Describe the morphology of the red blood cells.
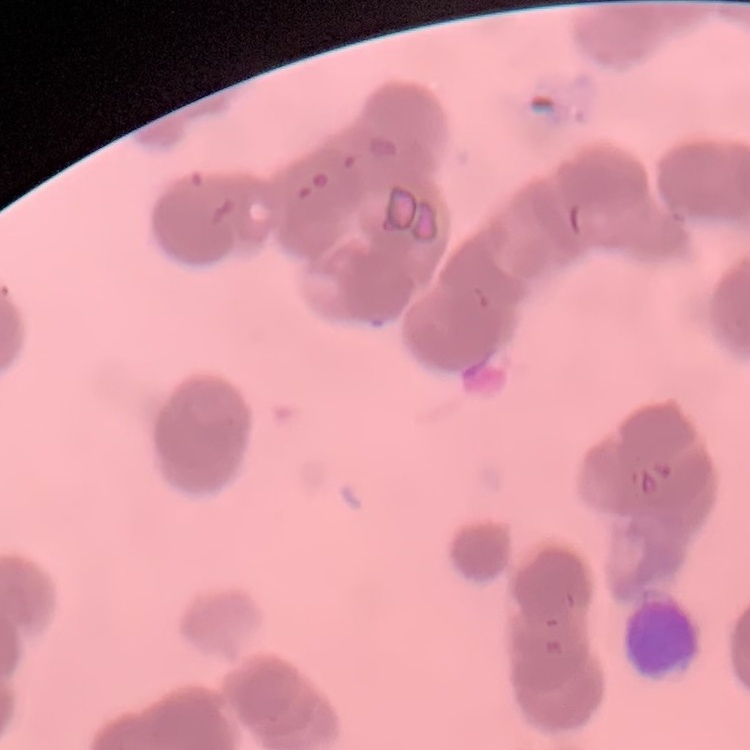
Rouleaux formation.

image type = one tile cut from a larger photomicrograph
stain = Field's or Giemsa
preparation = thin blood smear